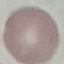
result = no malaria parasites seen
capture = smartphone camera at the microscope eyepiece
stain = Giemsa
preparation = thin blood film
image type = automatically extracted cell patch, resized to 64 × 64 pixels